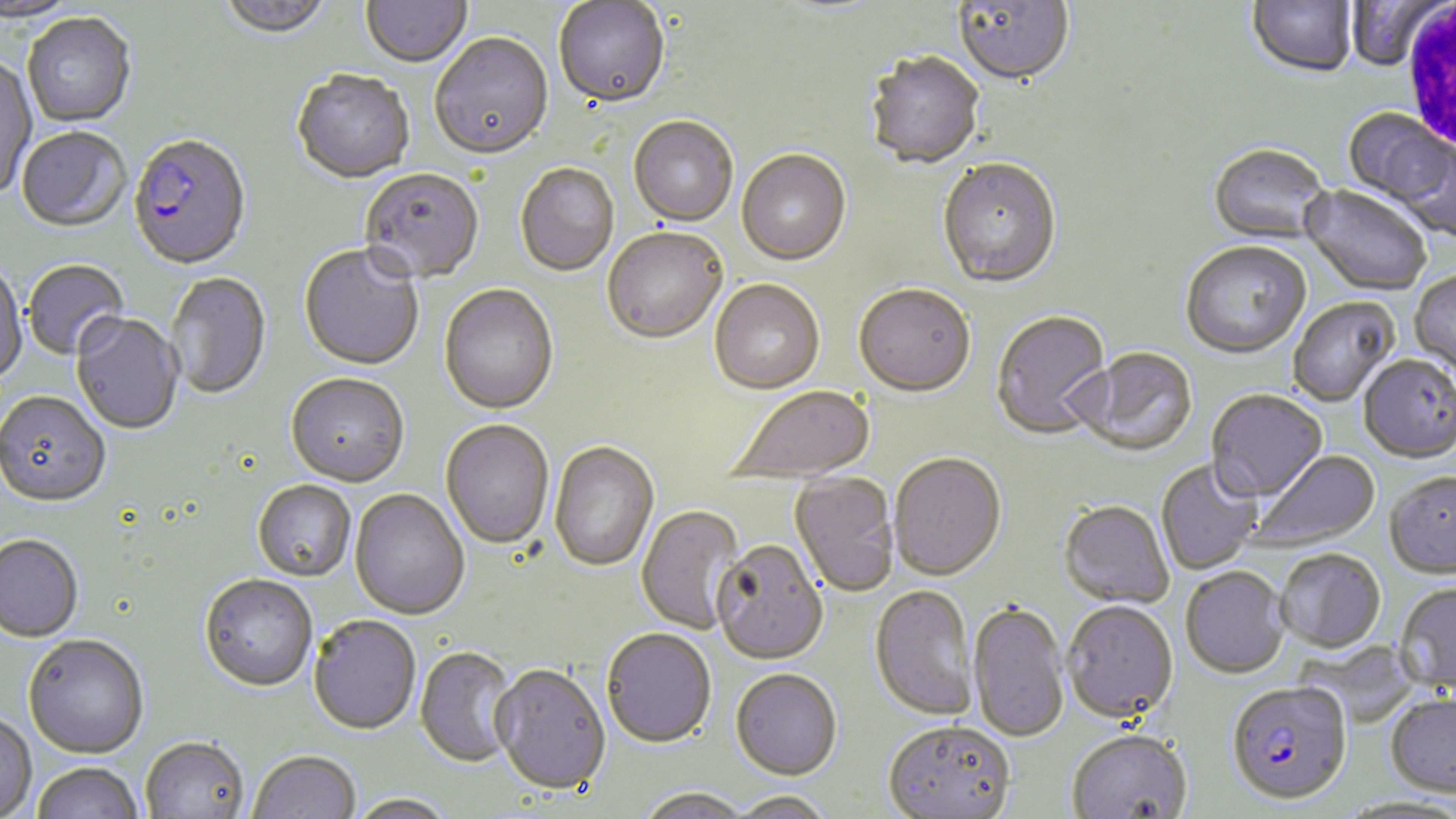

Plasmodium falciparum-infected red blood cell locations = approximate bounding boxes as [x1, y1, x2, y2] in pixels: [127, 135, 252, 273], [1227, 685, 1352, 808]
slide-level diagnosis = Plasmodium falciparum
field of view = single
stain = May-Grünwald-Giemsa
preparation = thin blood smear
magnification = 1000x
uninfected red blood cell locations = approximate bounding boxes as [x1, y1, x2, y2] in pixels: [0, 0, 82, 25], [218, 0, 334, 42], [1248, 0, 1357, 81], [361, 1, 472, 70], [771, 1, 889, 19], [953, 1, 1075, 88], [1346, 1, 1445, 72], [554, 2, 670, 111], [22, 15, 136, 129], [430, 35, 554, 163], [864, 53, 985, 171], [0, 57, 38, 200], [292, 72, 414, 185], [1343, 109, 1452, 208], [628, 118, 738, 228], [17, 129, 132, 234], [1396, 141, 1455, 241], [1207, 145, 1333, 247], [736, 152, 851, 268], [937, 160, 1062, 290], [515, 164, 619, 277], [359, 170, 484, 286], [1300, 186, 1431, 297], [602, 230, 727, 347], [1180, 242, 1311, 361], [298, 245, 424, 373], [23, 260, 130, 362], [0, 262, 27, 387], [1410, 271, 1456, 378], [165, 273, 271, 401], [709, 281, 825, 396], [438, 285, 559, 417], [854, 287, 976, 400], [1289, 298, 1400, 408], [991, 311, 1113, 441], [72, 314, 183, 436], [1073, 349, 1198, 458], [1358, 357, 1456, 466], [286, 376, 409, 489], [727, 386, 876, 485], [1206, 391, 1328, 505], [0, 393, 111, 510], [440, 421, 554, 550], [549, 442, 659, 573], [1249, 450, 1381, 553], [888, 454, 1008, 583], [1156, 460, 1263, 574], [788, 473, 900, 599], [1384, 475, 1456, 581], [253, 482, 356, 583], [349, 489, 470, 622], [1058, 502, 1174, 610], [636, 504, 747, 634], [0, 536, 83, 645], [711, 542, 829, 667], [1276, 551, 1386, 655], [1181, 569, 1289, 681], [199, 576, 317, 694], [1394, 585, 1456, 696], [868, 586, 980, 723], [1062, 603, 1178, 727], [968, 604, 1070, 746], [308, 618, 422, 737], [601, 630, 716, 750], [23, 636, 149, 761], [414, 647, 521, 768], [490, 666, 610, 797], [731, 671, 842, 782], [1385, 696, 1456, 801], [0, 714, 37, 819], [882, 724, 1016, 819], [1067, 733, 1192, 819], [140, 739, 249, 819], [248, 752, 360, 819], [32, 763, 143, 819], [636, 789, 753, 819], [730, 792, 835, 819], [348, 794, 458, 819]
image size = 1456×819 pixels
modality = light microscopy
white blood cell locations = approximate bounding boxes as [x1, y1, x2, y2] in pixels: [1402, 1, 1456, 152]